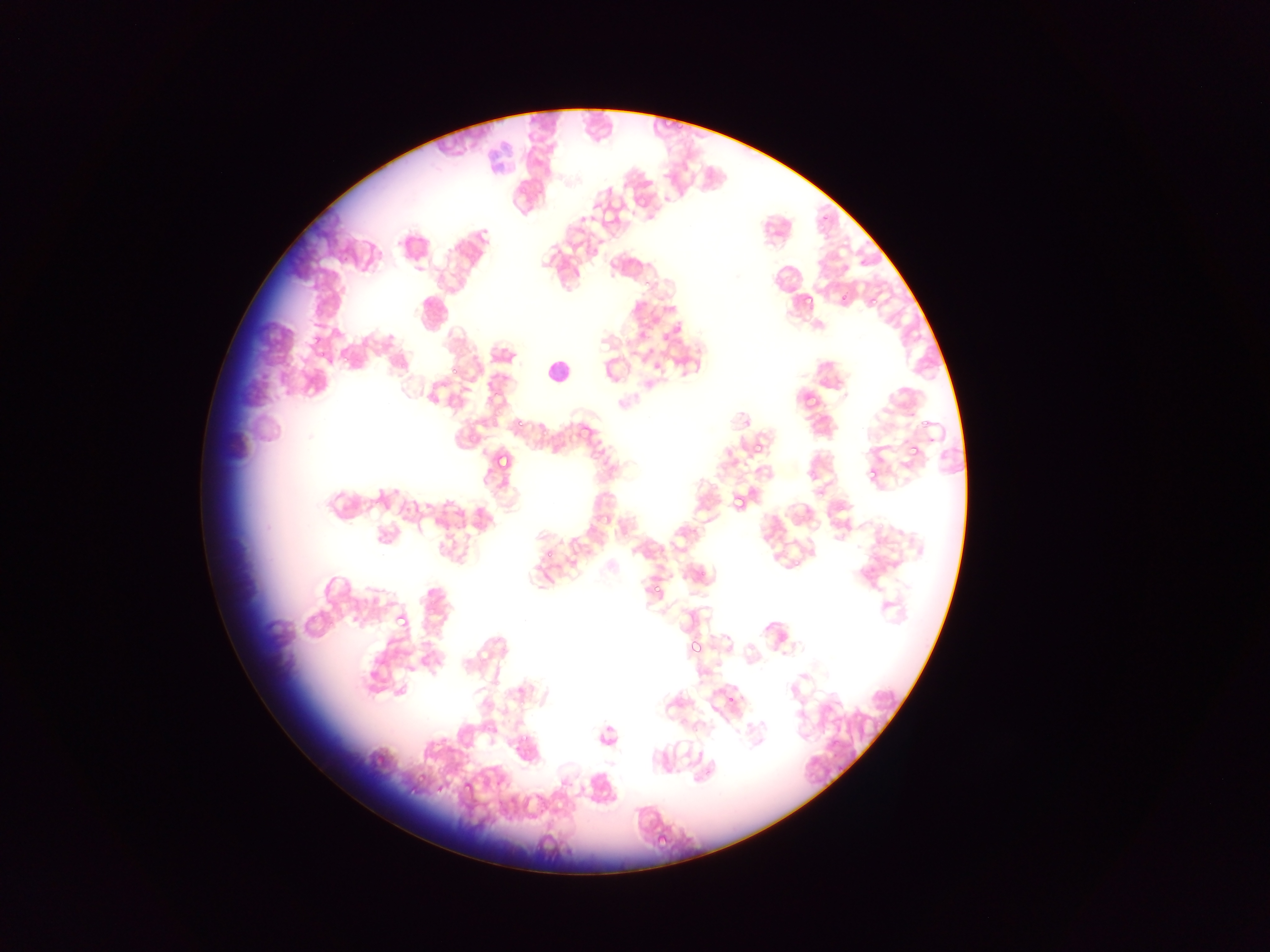
leukocyte_locations: 'approximate bounding boxes as [left, top, right, bottom] in pixels: [538, 353, 568, 385]'
preparation: thin blood smear
capture: mobile-phone photograph through a microscope
image_size: 1270×952 pixels
field_of_view: single
plasmodium_parasite_locations: 'approximate bounding boxes as [left, top, right, bottom] in pixels: [816, 211, 832, 228], [857, 255, 875, 270], [862, 286, 883, 314], [797, 291, 813, 307], [486, 378, 508, 402], [510, 416, 528, 433], [752, 441, 767, 458], [902, 443, 917, 458], [493, 450, 514, 474], [857, 464, 874, 479], [723, 484, 747, 519], [450, 503, 467, 522], [649, 572, 670, 594], [389, 614, 411, 630], [687, 638, 706, 659], [726, 692, 740, 707], [459, 775, 479, 797], [407, 783, 421, 798], [654, 832, 675, 851]'
country: Ghana